Assess this cell for malaria.
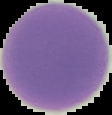

Uninfected.

Summary:
  - Image type: cell region segmented out of the field of view; surrounding area masked to black
  - Image size: 112×115 pixels
  - Preparation: thin blood smear